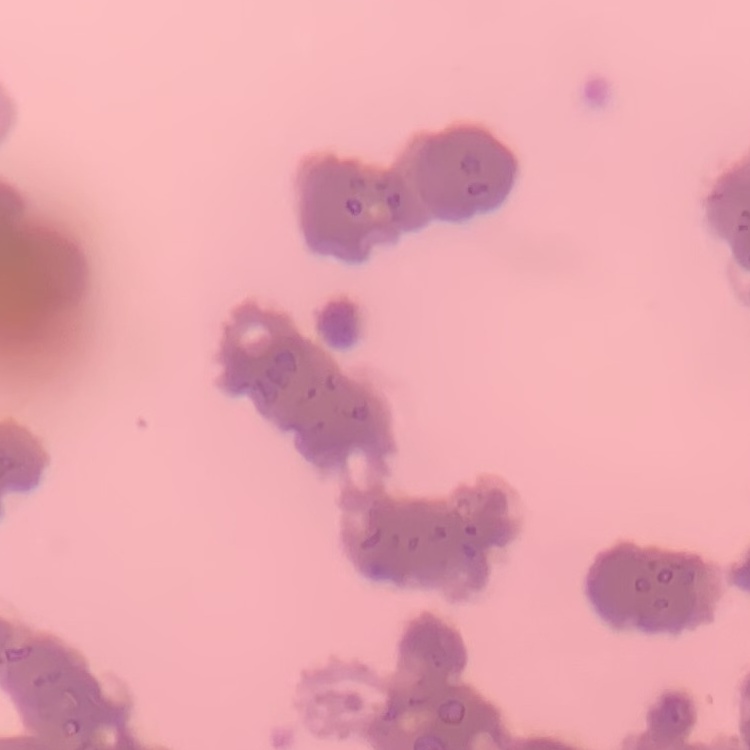

erythrocyte morphology = rouleaux formation
preparation = thin peripheral smear
stain = Field's or Giemsa
image type = square crop of a larger photomicrograph